Classify this cell by malaria status.
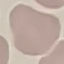
It is uninfected.

Summary:
  - Preparation: thin blood film
  - Stain: Giemsa
  - Image type: automatically extracted cell patch, resized to 64 × 64 pixels
  - Capture: smartphone through the microscope eyepiece